Locate every Plasmodium parasite.
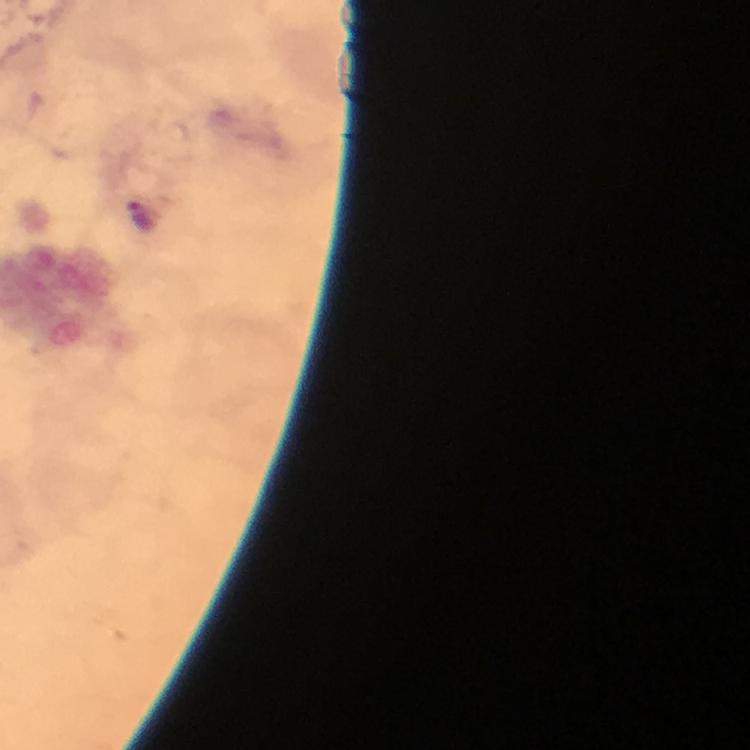

Approximate object centers, in pixels from the top-left corner.
Plasmodium parasites: (x=141, y=218).

magnification = 100x
context = from a malaria diagnostic workup
immersion oil = applied
capture = smartphone photograph through a microscope
stain = Giemsa
cropped from = one field of view
preparation = thick blood smear
image size = 750×750 pixels